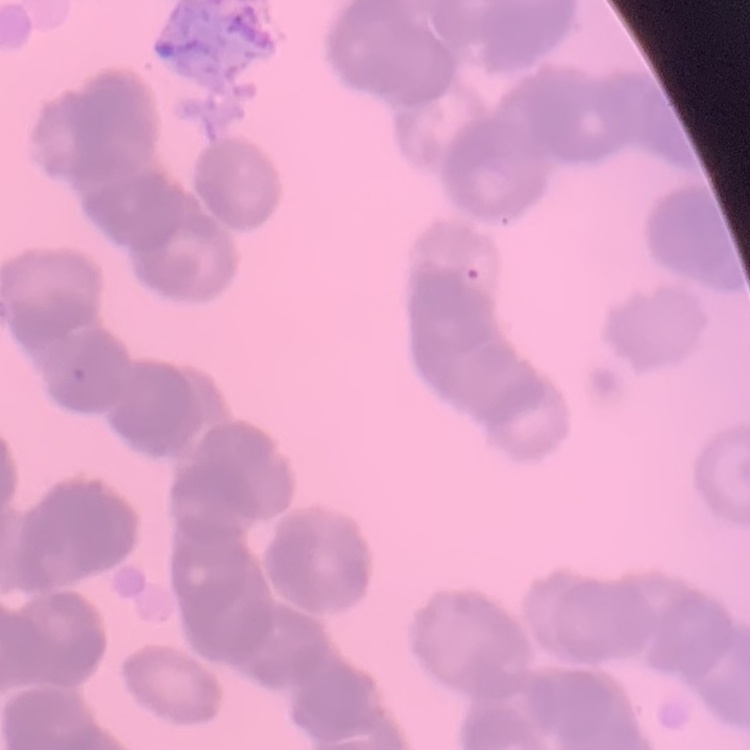
Summary:
  - Erythrocyte morphology: rouleaux formation
  - Stain: Field's or Giemsa
  - Preparation: thin blood film
  - Image type: square crop of a larger photomicrograph